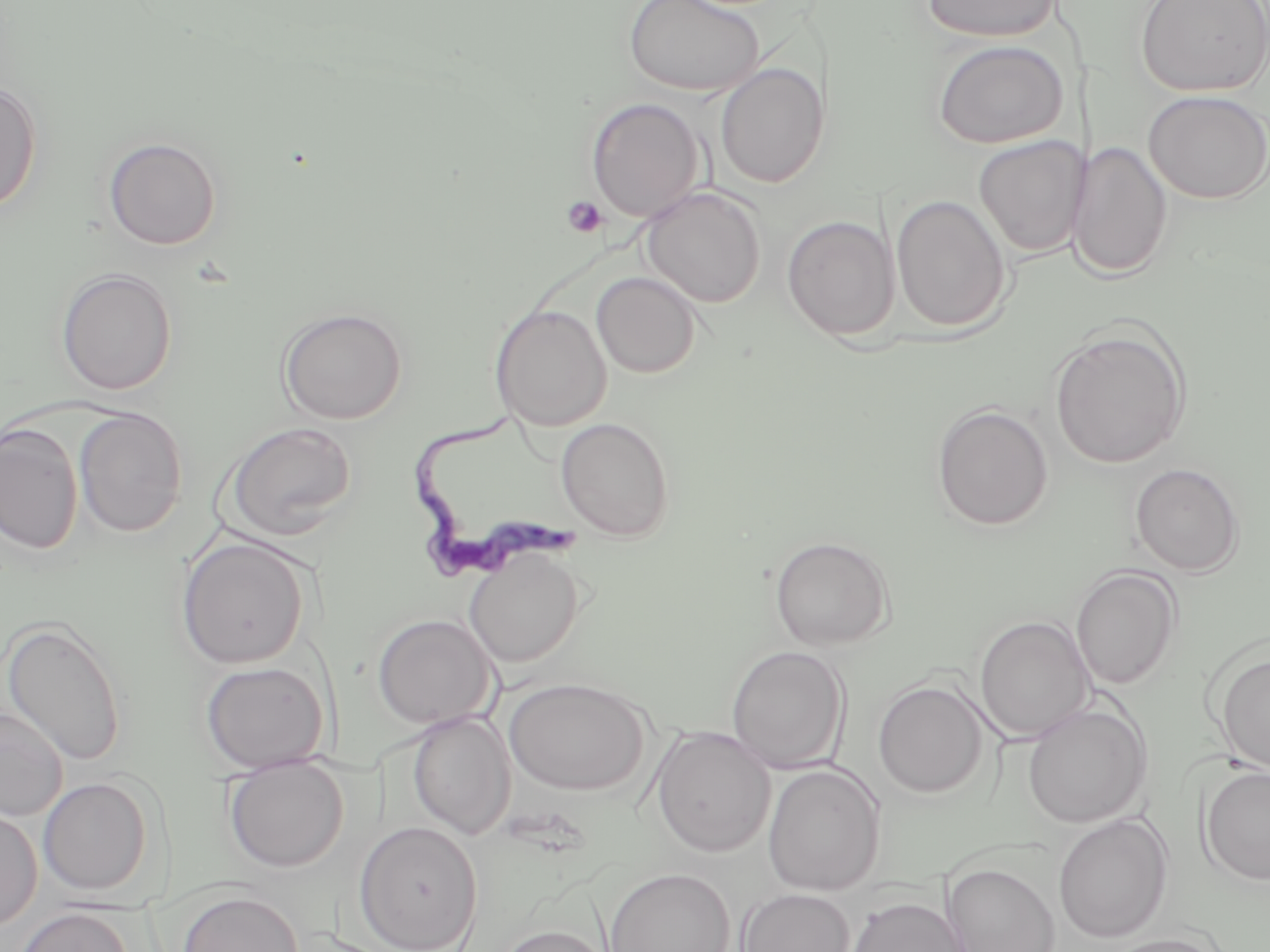
{
  "slide_level_diagnosis": "Trypanosoma brucei",
  "preparation": "thin blood film",
  "trypanosoma_brucei_locations": "approximate bounding boxes as (x1, y1, x2, y2) in pixels: (408, 405, 583, 582)",
  "magnification": "1000x",
  "platelet_locations": "approximate bounding boxes as (x1, y1, x2, y2) in pixels: (561, 196, 609, 239)",
  "modality": "optical microscopy",
  "image_size": "1270×952 pixels",
  "field_of_view": "one of a larger specimen",
  "uninfected_red_blood_cell_locations": "approximate bounding boxes as (x1, y1, x2, y2) in pixels: (622, 0, 764, 97), (921, 0, 1062, 43), (1133, 0, 1270, 97), (932, 39, 1069, 148), (716, 63, 829, 188), (0, 79, 43, 214), (1143, 90, 1270, 204), (585, 97, 706, 223), (973, 135, 1087, 258), (103, 136, 223, 250), (1073, 141, 1172, 280), (641, 186, 766, 308), (891, 195, 1011, 332), (781, 215, 900, 340), (55, 267, 177, 395), (592, 271, 701, 379), (490, 304, 612, 431), (277, 307, 408, 424), (1050, 327, 1190, 469), (931, 403, 1054, 532), (73, 408, 188, 537), (556, 417, 676, 541), (221, 421, 359, 542), (0, 423, 83, 555), (1130, 463, 1244, 576), (769, 535, 894, 651), (175, 536, 311, 669), (463, 548, 585, 668), (1071, 567, 1182, 691), (372, 613, 497, 729), (973, 615, 1093, 742), (1, 617, 128, 769), (726, 645, 850, 773), (1214, 651, 1270, 775), (199, 660, 331, 773), (504, 677, 651, 796), (873, 679, 989, 798), (1022, 703, 1152, 829), (0, 707, 68, 823), (407, 712, 517, 839), (651, 726, 776, 857), (223, 758, 349, 873), (1198, 763, 1270, 886), (763, 764, 886, 896), (38, 777, 155, 896), (0, 804, 42, 929), (1052, 813, 1173, 943), (354, 821, 483, 952), (944, 862, 1060, 952), (604, 868, 736, 952), (737, 887, 855, 952), (177, 890, 304, 952), (846, 896, 968, 952), (12, 907, 134, 952), (495, 923, 614, 952), (1099, 932, 1230, 952)",
  "stain": "May-Grünwald-Giemsa"
}